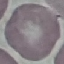
Result: negative for malaria parasites. Thin blood smear. Automatically extracted cell patch, resized to 64 × 64 pixels. Giemsa stain. Photographed with a smartphone camera at the microscope eyepiece.